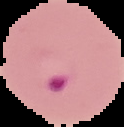

Image is 124×127 pixels. From a thin blood smear. Malaria status: parasitized. The area outside the segmented cell region is set to black.